Report the malaria status of this cell.
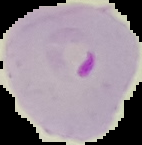

It is parasitized.

Summary:
  - Image type: segmented cell region on a black background
  - Preparation: thin blood smear
  - Image size: 142×145 pixels